State the blood parasite species.
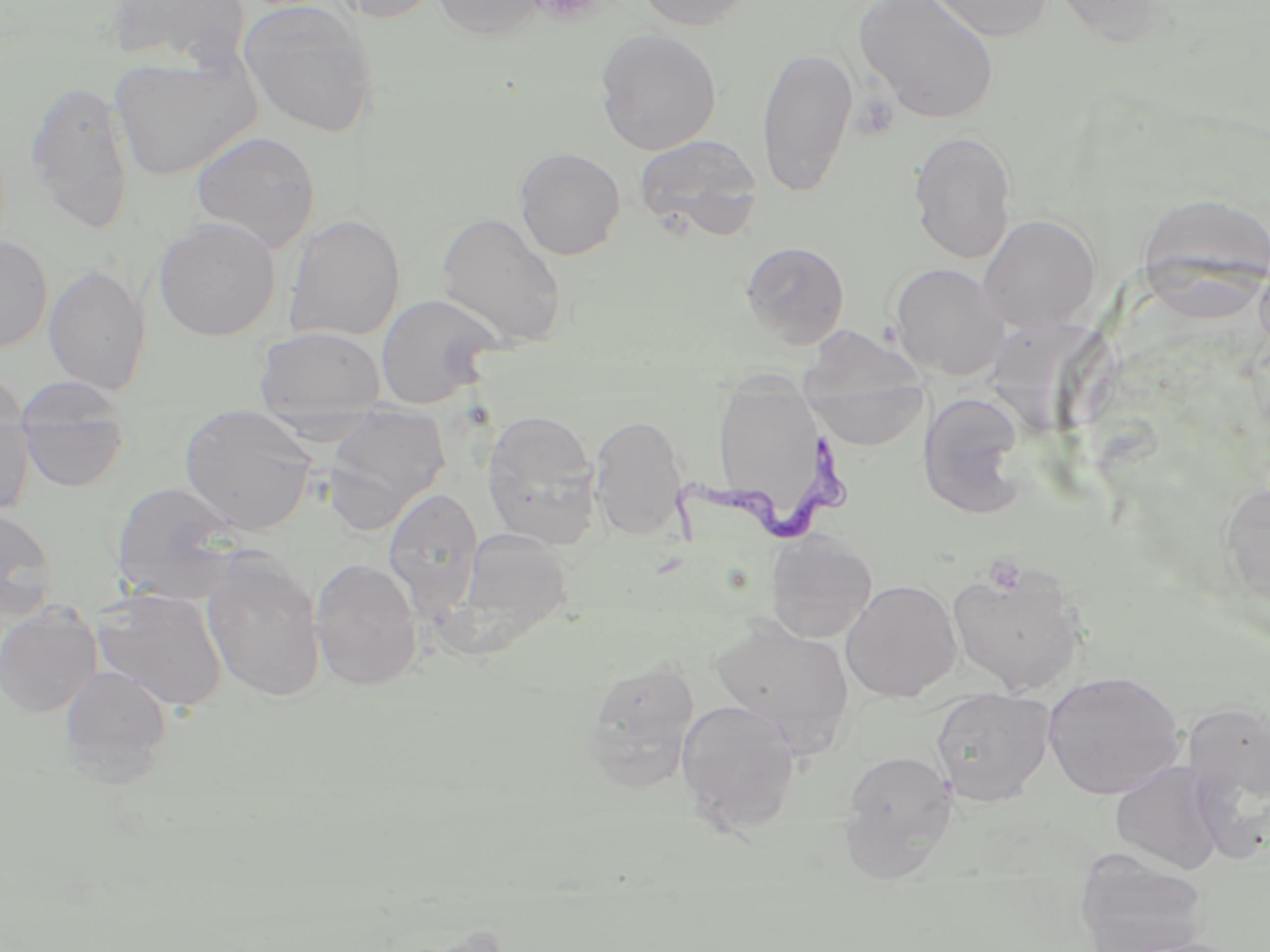
Trypanosoma brucei.

Summary:
  - Coordinate format: approximate bounding boxes as (x1, y1, x2, y2) in pixels
  - Trypanosoma brucei locations: (667, 425, 867, 556)
  - Uninfected red blood cell locations: (104, 0, 250, 68), (328, 0, 444, 24), (431, 0, 545, 40), (635, 0, 755, 30), (854, 0, 999, 124), (923, 0, 1054, 41), (1045, 0, 1172, 40), (238, 2, 380, 139), (595, 28, 722, 155), (756, 46, 858, 197), (108, 54, 260, 180), (23, 79, 136, 235), (190, 130, 320, 253), (908, 131, 1017, 265), (634, 134, 763, 241), (514, 147, 625, 260), (1136, 192, 1270, 308), (435, 211, 568, 349), (977, 213, 1101, 333), (283, 214, 405, 343), (153, 217, 281, 341), (0, 235, 53, 352), (741, 241, 850, 348), (889, 262, 1009, 380), (43, 264, 151, 396), (375, 293, 501, 409), (254, 325, 387, 416), (802, 328, 929, 443), (0, 366, 27, 429), (11, 376, 128, 428), (711, 376, 832, 528), (918, 391, 1031, 519), (178, 407, 318, 535), (322, 407, 451, 529), (16, 408, 131, 493), (481, 408, 602, 549), (0, 411, 35, 518), (589, 414, 688, 540), (1218, 479, 1270, 613), (109, 481, 247, 604), (383, 487, 484, 616), (0, 507, 59, 619), (454, 528, 574, 647), (765, 532, 878, 643), (202, 553, 327, 703), (309, 557, 423, 692), (947, 563, 1087, 695), (840, 578, 962, 702), (91, 587, 228, 712), (0, 604, 103, 718), (710, 616, 855, 756), (582, 657, 701, 791), (58, 664, 172, 785), (1042, 670, 1186, 800), (930, 686, 1056, 807), (675, 699, 803, 834), (1181, 700, 1270, 822), (838, 747, 958, 870), (1109, 760, 1225, 874), (1073, 848, 1212, 952)
  - Stain: May-Grünwald-Giemsa
  - Modality: optical microscopy
  - Preparation: thin blood film
  - Field of view: single
  - Magnification: 1000x
  - Image size: 1270×952 pixels